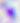

{
  "magnification": "400x",
  "identification": "Toxoplasma gondii",
  "modality": "micrograph"
}